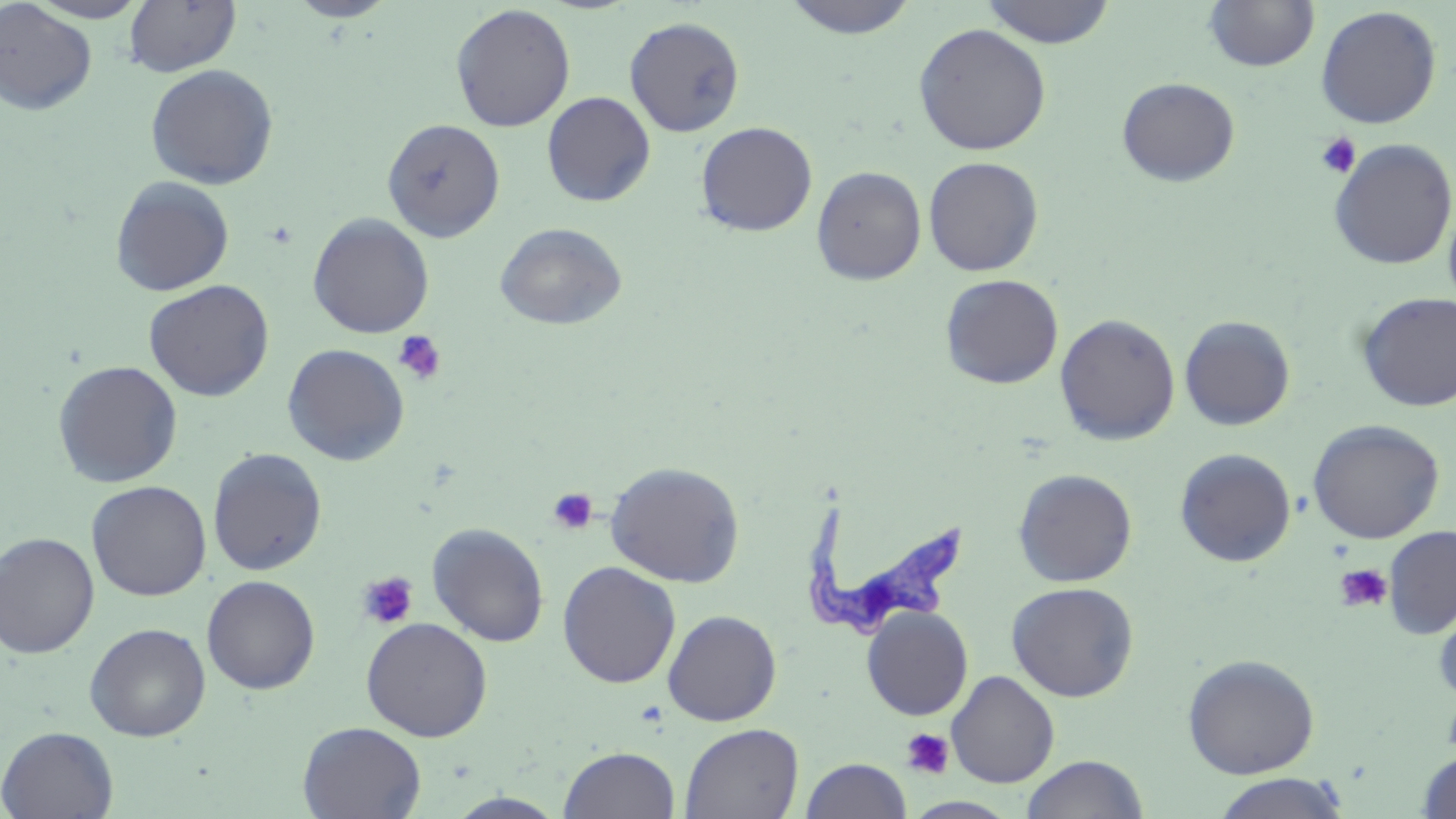

slide-level diagnosis = Trypanosoma brucei
field of view = one of a larger specimen
image size = 1456×819 pixels
platelet locations = approximate bounding boxes as (x1,y1)-(x2,y2) corner pairs in pixels: (1315,132)-(1362,179), (392,330)-(446,385), (546,487)-(598,535), (1333,564)-(1393,613), (356,570)-(420,631), (900,727)-(955,780)
uninfected red blood cell locations = approximate bounding boxes as (x1,y1)-(x2,y2) corner pairs in pixels: (26,0)-(150,22), (287,0)-(399,21), (781,0)-(919,40), (980,0)-(1116,48), (0,1)-(97,116), (124,1)-(241,77), (1203,1)-(1319,73), (450,4)-(576,132), (1315,5)-(1442,129), (625,16)-(745,138), (912,23)-(1052,156), (145,64)-(279,190), (1117,77)-(1240,187), (541,91)-(656,207), (382,118)-(505,241), (695,121)-(818,236), (1327,138)-(1456,270), (923,156)-(1044,276), (811,165)-(926,285), (110,176)-(235,296), (1443,193)-(1456,314), (307,213)-(434,339), (495,222)-(627,330), (940,273)-(1063,389), (143,279)-(275,402), (1356,292)-(1456,412), (1055,313)-(1181,445), (1179,316)-(1295,430), (282,343)-(410,466), (52,360)-(183,488), (1308,419)-(1445,544), (207,447)-(327,576), (1174,448)-(1296,567), (604,460)-(746,587), (1012,468)-(1137,587), (86,480)-(211,601), (426,522)-(550,647), (1382,526)-(1456,639), (0,531)-(100,659), (557,561)-(681,688), (201,574)-(321,694), (1006,581)-(1139,702), (1434,597)-(1456,707), (861,606)-(974,721), (662,609)-(782,726), (360,617)-(493,742), (85,622)-(211,742), (1183,653)-(1320,778), (946,670)-(1060,787), (297,721)-(426,819), (679,723)-(804,819), (0,726)-(119,819), (559,745)-(680,818), (1416,749)-(1456,819), (1020,754)-(1149,819), (800,757)-(912,819), (1210,772)-(1350,818), (445,792)-(569,818), (904,797)-(1021,818)
preparation = thin blood smear
modality = light microscopy
stain = May-Grünwald-Giemsa
magnification = 1000x
Trypanosoma brucei locations = approximate bounding boxes as (x1,y1)-(x2,y2) corner pairs in pixels: (802,496)-(973,640)